State the blood parasite species.
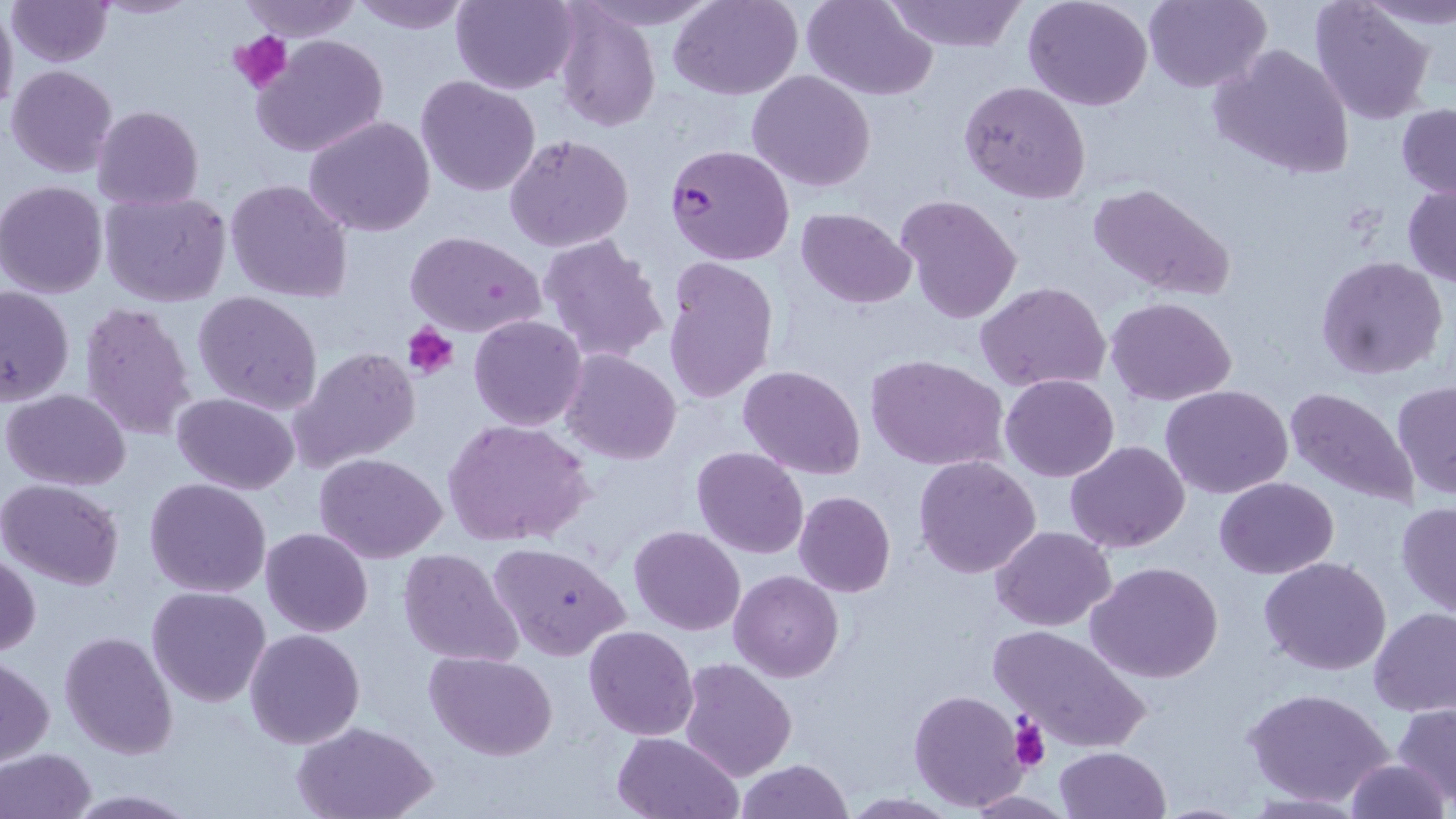

Plasmodium falciparum.

Approximate bounding boxes as named x1/y1/x2/y2 corners in pixels. Plasmodium falciparum-infected red blood cell locations: (x1=663, y1=143, x2=795, y2=267). Uninfected red blood cell locations: (x1=239, y1=0, x2=360, y2=41), (x1=348, y1=0, x2=471, y2=35), (x1=451, y1=0, x2=581, y2=95), (x1=579, y1=0, x2=720, y2=30), (x1=670, y1=0, x2=803, y2=100), (x1=801, y1=0, x2=937, y2=99), (x1=884, y1=0, x2=1026, y2=53), (x1=1145, y1=0, x2=1272, y2=93), (x1=1310, y1=0, x2=1435, y2=124), (x1=5, y1=1, x2=113, y2=66), (x1=1022, y1=1, x2=1153, y2=111), (x1=0, y1=4, x2=18, y2=118), (x1=553, y1=4, x2=660, y2=133), (x1=252, y1=33, x2=389, y2=158), (x1=1209, y1=43, x2=1355, y2=179), (x1=7, y1=65, x2=120, y2=179), (x1=746, y1=70, x2=877, y2=193), (x1=415, y1=75, x2=542, y2=198), (x1=958, y1=81, x2=1091, y2=204), (x1=1396, y1=104, x2=1456, y2=199), (x1=93, y1=106, x2=203, y2=210), (x1=303, y1=116, x2=436, y2=239), (x1=504, y1=134, x2=635, y2=253), (x1=224, y1=178, x2=353, y2=304), (x1=0, y1=181, x2=110, y2=299), (x1=1087, y1=181, x2=1236, y2=300), (x1=1402, y1=181, x2=1456, y2=288), (x1=98, y1=190, x2=231, y2=307), (x1=894, y1=194, x2=1022, y2=325), (x1=796, y1=207, x2=918, y2=308), (x1=403, y1=229, x2=547, y2=338), (x1=537, y1=232, x2=670, y2=365), (x1=1315, y1=256, x2=1448, y2=381), (x1=661, y1=258, x2=778, y2=406), (x1=975, y1=281, x2=1111, y2=391), (x1=0, y1=284, x2=74, y2=406), (x1=192, y1=290, x2=324, y2=415), (x1=1106, y1=297, x2=1237, y2=404), (x1=77, y1=301, x2=199, y2=442), (x1=468, y1=315, x2=587, y2=430), (x1=289, y1=347, x2=422, y2=474), (x1=560, y1=348, x2=682, y2=465), (x1=864, y1=354, x2=1010, y2=474), (x1=739, y1=366, x2=866, y2=480), (x1=1000, y1=373, x2=1118, y2=481), (x1=1393, y1=379, x2=1456, y2=499), (x1=1161, y1=384, x2=1294, y2=498), (x1=1285, y1=386, x2=1420, y2=510), (x1=3, y1=389, x2=132, y2=490), (x1=172, y1=391, x2=299, y2=495), (x1=443, y1=417, x2=593, y2=549), (x1=1064, y1=441, x2=1190, y2=553), (x1=691, y1=445, x2=808, y2=560), (x1=315, y1=453, x2=447, y2=564), (x1=914, y1=455, x2=1041, y2=579), (x1=0, y1=477, x2=125, y2=590), (x1=1214, y1=477, x2=1339, y2=579), (x1=144, y1=478, x2=273, y2=599), (x1=793, y1=490, x2=896, y2=596), (x1=1396, y1=501, x2=1456, y2=617), (x1=629, y1=525, x2=745, y2=637), (x1=261, y1=526, x2=374, y2=638), (x1=991, y1=526, x2=1113, y2=630), (x1=488, y1=541, x2=629, y2=662), (x1=398, y1=547, x2=524, y2=666), (x1=1, y1=554, x2=40, y2=657), (x1=1258, y1=556, x2=1391, y2=676), (x1=1087, y1=562, x2=1223, y2=683), (x1=729, y1=570, x2=843, y2=681), (x1=147, y1=586, x2=272, y2=708), (x1=1369, y1=607, x2=1456, y2=716), (x1=991, y1=624, x2=1149, y2=753), (x1=584, y1=625, x2=698, y2=740), (x1=243, y1=628, x2=366, y2=748), (x1=59, y1=630, x2=178, y2=759), (x1=425, y1=650, x2=556, y2=760), (x1=1, y1=657, x2=52, y2=765), (x1=678, y1=658, x2=796, y2=781), (x1=1243, y1=686, x2=1394, y2=807), (x1=908, y1=688, x2=1030, y2=811), (x1=1393, y1=703, x2=1456, y2=805), (x1=292, y1=720, x2=437, y2=819), (x1=612, y1=731, x2=742, y2=818), (x1=1054, y1=746, x2=1170, y2=819), (x1=0, y1=748, x2=97, y2=819), (x1=735, y1=758, x2=854, y2=818), (x1=1344, y1=758, x2=1450, y2=818), (x1=965, y1=789, x2=1076, y2=817), (x1=60, y1=790, x2=202, y2=817), (x1=840, y1=794, x2=962, y2=818). Platelet locations: (x1=229, y1=29, x2=294, y2=91), (x1=403, y1=322, x2=460, y2=378), (x1=1008, y1=716, x2=1052, y2=771). Optical microscopy. Thin blood film. May-Grünwald-Giemsa-stained preparation. 1000x magnification. Image is 1456×819 pixels. One field of a larger specimen.